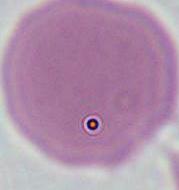
{
  "modality": "photomicrograph",
  "identification": "erythrocyte",
  "magnification": "1000x"
}